Assess this cell for malaria.
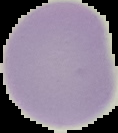
It is uninfected.

image type = segmented cell region with the area outside set to black
image size = 118×133 pixels
preparation = thin blood film